Name the blood parasite species.
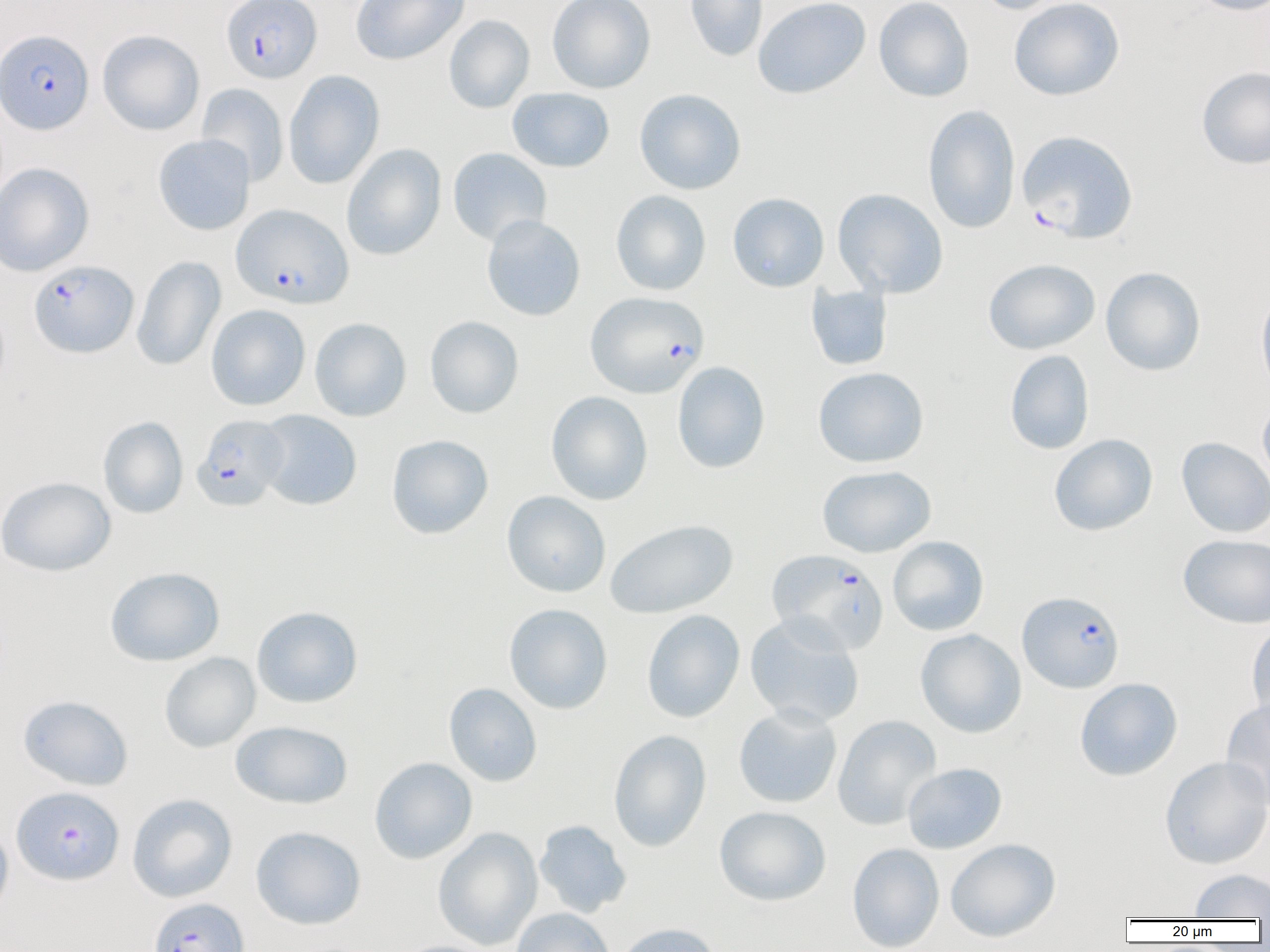

Plasmodium falciparum.

Summary:
  - Coordinate format: approximate bounding boxes as (x1,y1)-(x2,y2) corner pairs in pixels
  - Plasmodium falciparum-infected red blood cell locations: (221,0)-(322,83), (0,29)-(93,134), (1017,130)-(1138,243), (231,204)-(353,309), (29,259)-(138,358), (585,291)-(709,398), (192,414)-(290,511), (768,548)-(889,654), (1017,590)-(1125,693), (12,786)-(124,885), (148,897)-(249,952)
  - Uninfected red blood cell locations: (351,0)-(469,65), (547,0)-(655,93), (684,0)-(768,62), (752,0)-(871,99), (873,0)-(974,102), (973,0)-(1073,15), (1008,0)-(1125,101), (1187,0)-(1270,15), (444,15)-(535,113), (98,29)-(205,135), (1196,65)-(1270,170), (283,70)-(385,189), (196,83)-(289,187), (507,87)-(615,172), (634,88)-(746,195), (923,105)-(1021,234), (153,134)-(255,235), (341,143)-(446,261), (448,147)-(552,246), (0,162)-(94,276), (832,188)-(949,298), (610,190)-(711,296), (727,192)-(829,292), (481,214)-(586,322), (131,255)-(226,371), (983,258)-(1100,355), (1100,267)-(1205,376), (806,283)-(893,371), (1255,286)-(1270,401), (206,304)-(310,411), (424,316)-(524,418), (309,317)-(412,422), (1005,349)-(1095,455), (672,361)-(770,473), (813,366)-(929,468), (545,391)-(653,505), (1257,396)-(1270,493), (256,410)-(362,510), (98,416)-(189,519), (1049,433)-(1158,536), (386,434)-(494,539), (1176,437)-(1270,538), (817,465)-(936,558), (0,476)-(116,577), (502,490)-(611,597), (605,518)-(738,619), (1178,534)-(1269,629), (888,536)-(989,636), (105,566)-(225,666), (503,603)-(613,714), (252,606)-(363,708), (641,609)-(745,723), (744,615)-(865,728), (1246,621)-(1270,729), (916,629)-(1026,738), (159,652)-(260,753), (1074,678)-(1183,781), (443,683)-(542,787), (18,695)-(134,791), (1220,698)-(1270,808), (733,704)-(843,808), (832,714)-(942,830), (230,720)-(353,809), (608,729)-(711,851), (1159,755)-(1270,869), (369,757)-(477,864), (902,763)-(1006,854), (127,794)-(237,902), (714,805)-(831,906), (534,820)-(632,917), (0,821)-(13,922), (250,826)-(366,929), (433,827)-(543,950), (945,838)-(1061,942), (847,843)-(945,951), (1189,869)-(1269,919), (511,907)-(615,952), (614,923)-(723,952), (392,939)-(497,952)
  - Magnification: 1000x
  - Preparation: thin blood smear
  - Modality: light microscopy
  - Field of view: single
  - Image size: 1270×952 pixels